State the blood parasite species.
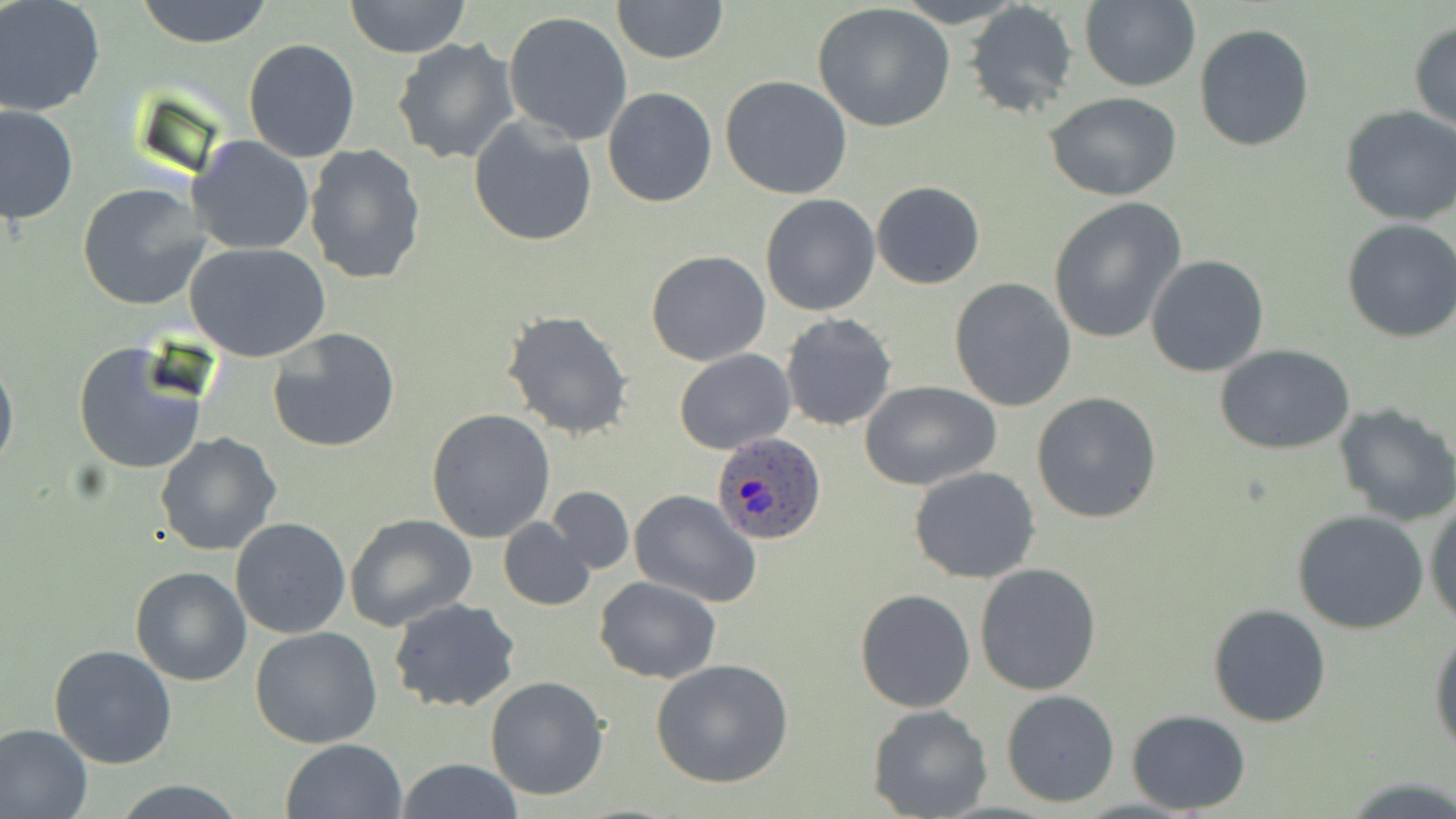

Plasmodium ovale.

Summary:
  - Coordinate format: approximate bounding boxes as named x1/y1/x2/y2 corners in pixels
  - Plasmodium ovale-infected red blood cell locations: (x1=714, y1=433, x2=825, y2=544)
  - Uninfected red blood cell locations: (x1=134, y1=0, x2=275, y2=47), (x1=342, y1=0, x2=473, y2=58), (x1=610, y1=0, x2=729, y2=65), (x1=1079, y1=0, x2=1201, y2=93), (x1=0, y1=1, x2=105, y2=117), (x1=966, y1=3, x2=1080, y2=119), (x1=813, y1=4, x2=957, y2=134), (x1=503, y1=10, x2=634, y2=146), (x1=1409, y1=19, x2=1456, y2=131), (x1=1194, y1=22, x2=1318, y2=152), (x1=392, y1=36, x2=520, y2=166), (x1=243, y1=38, x2=360, y2=163), (x1=720, y1=76, x2=852, y2=200), (x1=603, y1=86, x2=718, y2=207), (x1=1045, y1=92, x2=1183, y2=202), (x1=0, y1=103, x2=78, y2=226), (x1=1339, y1=106, x2=1456, y2=226), (x1=468, y1=114, x2=599, y2=247), (x1=186, y1=136, x2=315, y2=256), (x1=304, y1=145, x2=428, y2=286), (x1=871, y1=181, x2=986, y2=289), (x1=77, y1=183, x2=210, y2=310), (x1=760, y1=193, x2=882, y2=316), (x1=1046, y1=198, x2=1185, y2=343), (x1=1341, y1=218, x2=1456, y2=343), (x1=185, y1=241, x2=331, y2=362), (x1=646, y1=250, x2=772, y2=366), (x1=1145, y1=255, x2=1270, y2=376), (x1=947, y1=278, x2=1077, y2=412), (x1=502, y1=309, x2=633, y2=440), (x1=779, y1=311, x2=898, y2=432), (x1=267, y1=327, x2=401, y2=451), (x1=72, y1=341, x2=208, y2=476), (x1=1216, y1=346, x2=1354, y2=454), (x1=675, y1=347, x2=794, y2=454), (x1=0, y1=352, x2=18, y2=477), (x1=862, y1=381, x2=1001, y2=490), (x1=1032, y1=391, x2=1163, y2=524), (x1=1333, y1=403, x2=1456, y2=528), (x1=427, y1=408, x2=558, y2=542), (x1=154, y1=433, x2=281, y2=557), (x1=909, y1=466, x2=1041, y2=584), (x1=546, y1=486, x2=634, y2=573), (x1=630, y1=491, x2=761, y2=607), (x1=1424, y1=497, x2=1456, y2=627), (x1=1292, y1=509, x2=1429, y2=633), (x1=344, y1=514, x2=476, y2=632), (x1=230, y1=517, x2=352, y2=639), (x1=498, y1=517, x2=597, y2=611), (x1=129, y1=544, x2=341, y2=668), (x1=974, y1=563, x2=1101, y2=695), (x1=130, y1=564, x2=252, y2=685), (x1=594, y1=575, x2=721, y2=685), (x1=855, y1=590, x2=974, y2=712), (x1=389, y1=598, x2=520, y2=714), (x1=1206, y1=603, x2=1332, y2=727), (x1=1428, y1=624, x2=1456, y2=759), (x1=249, y1=627, x2=383, y2=749), (x1=48, y1=643, x2=179, y2=769), (x1=652, y1=659, x2=794, y2=788), (x1=483, y1=675, x2=611, y2=802), (x1=1001, y1=689, x2=1120, y2=809), (x1=868, y1=705, x2=994, y2=819), (x1=1126, y1=709, x2=1250, y2=814), (x1=0, y1=721, x2=93, y2=819), (x1=282, y1=739, x2=406, y2=819), (x1=396, y1=759, x2=523, y2=818), (x1=110, y1=778, x2=247, y2=817)
  - Field of view: one of a larger specimen
  - Modality: light microscopy
  - Stain: May-Grünwald-Giemsa
  - Magnification: 1000x
  - Image size: 1456×819 pixels
  - Preparation: thin blood smear